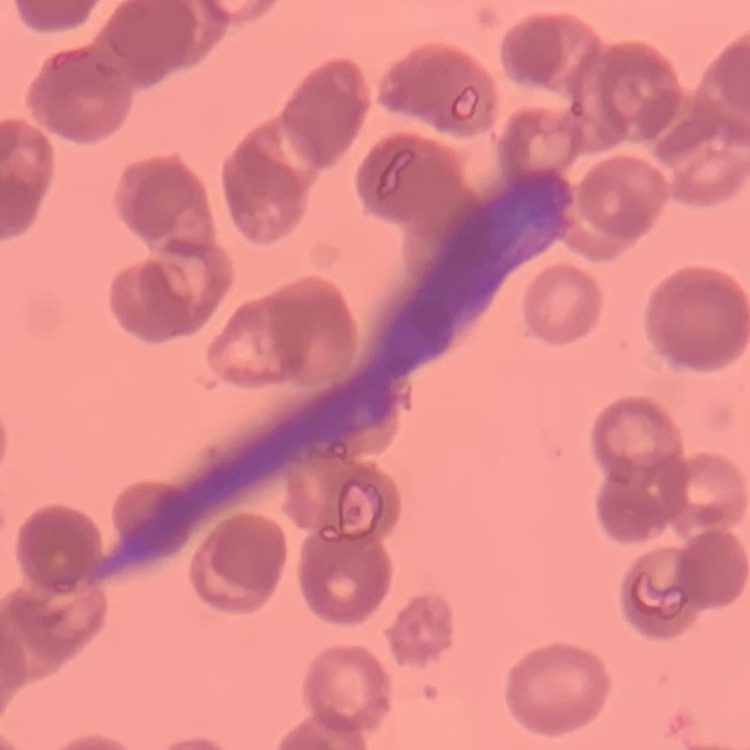

{
  "erythrocyte_morphology": "rouleaux formation",
  "stain": "Field's or Giemsa",
  "preparation": "thin blood smear",
  "image_type": "square crop of a larger photomicrograph"
}